State which parasite is depicted.
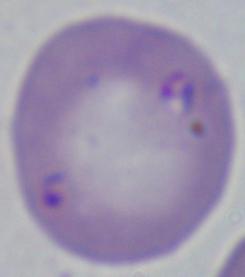
Babesia.

Summary:
  - Magnification: 1000x
  - Modality: micrograph